Assess the morphology of the erythrocytes.
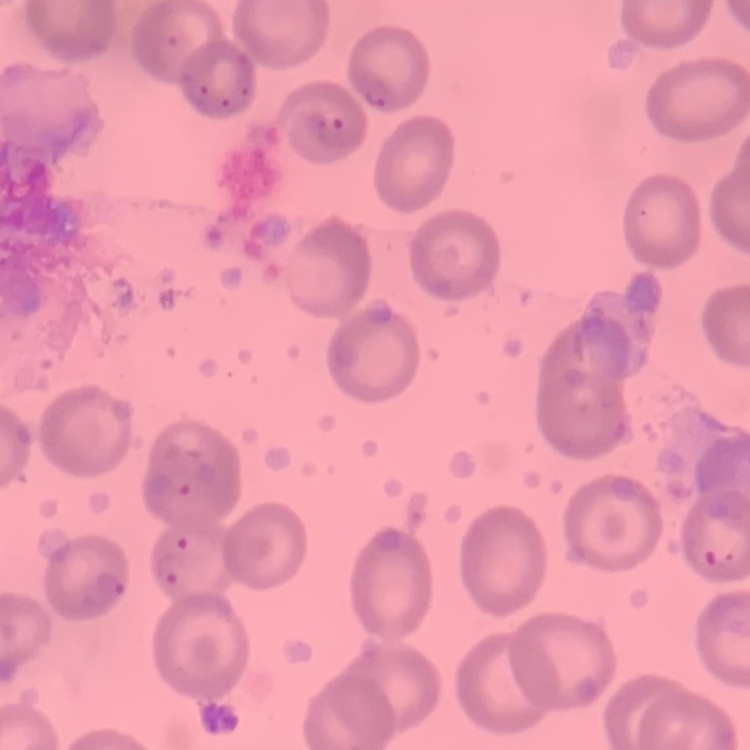
No rouleaux formation.

Summary:
  - Preparation: thin blood smear
  - Image type: one tile cut from a larger photomicrograph
  - Stain: Field's or Giemsa